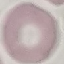
malaria status = uninfected
image type = cell patch, automatically extracted from a larger field of view and resized to 64 × 64 pixels
stain = Giemsa
capture = smartphone through the microscope eyepiece
preparation = thin blood film